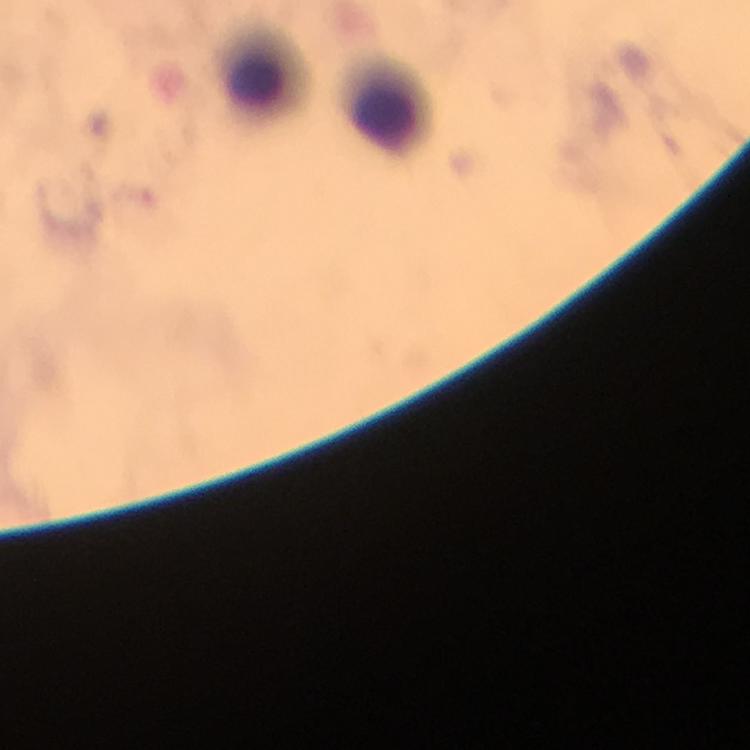
Plasmodium parasites = none seen
capture = smartphone photograph through a microscope
preparation = thick blood film
context = from a malaria diagnostic workup
image size = 750×750 pixels
magnification = 100x
leukocyte locations = approximate centers as {x, y} in pixels: {259, 79}, {388, 115}
immersion oil = applied
stain = Giemsa
cropped from = a single field of view